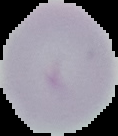
Summary:
  - Image type: segmented cell region on a black background
  - Image size: 118×136 pixels
  - Preparation: thin blood smear
  - Result: no malaria parasites seen